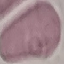

Summary:
  - Result: negative for malaria parasites
  - Capture: smartphone through the microscope eyepiece
  - Stain: Giemsa
  - Preparation: thin smear
  - Image type: automatically extracted cell patch, resized to 64 × 64 pixels